Report the malaria status of this cell.
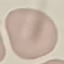
Uninfected.

image type = automatically extracted cell patch, resized to 64 × 64 pixels
capture = smartphone camera at the microscope eyepiece
stain = Giemsa
preparation = thin smear